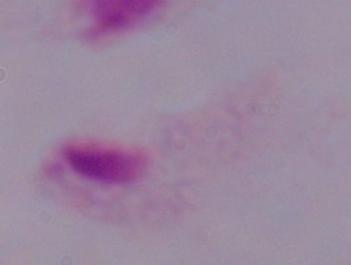
modality = micrograph
identification = trichomonad
magnification = 1000x